Report the malaria status of this cell.
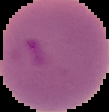

It is parasitized.

image size = 109×112 pixels
image type = cell region segmented out of the field of view; surrounding area masked to black
preparation = thin blood smear